Identify the blood parasite species.
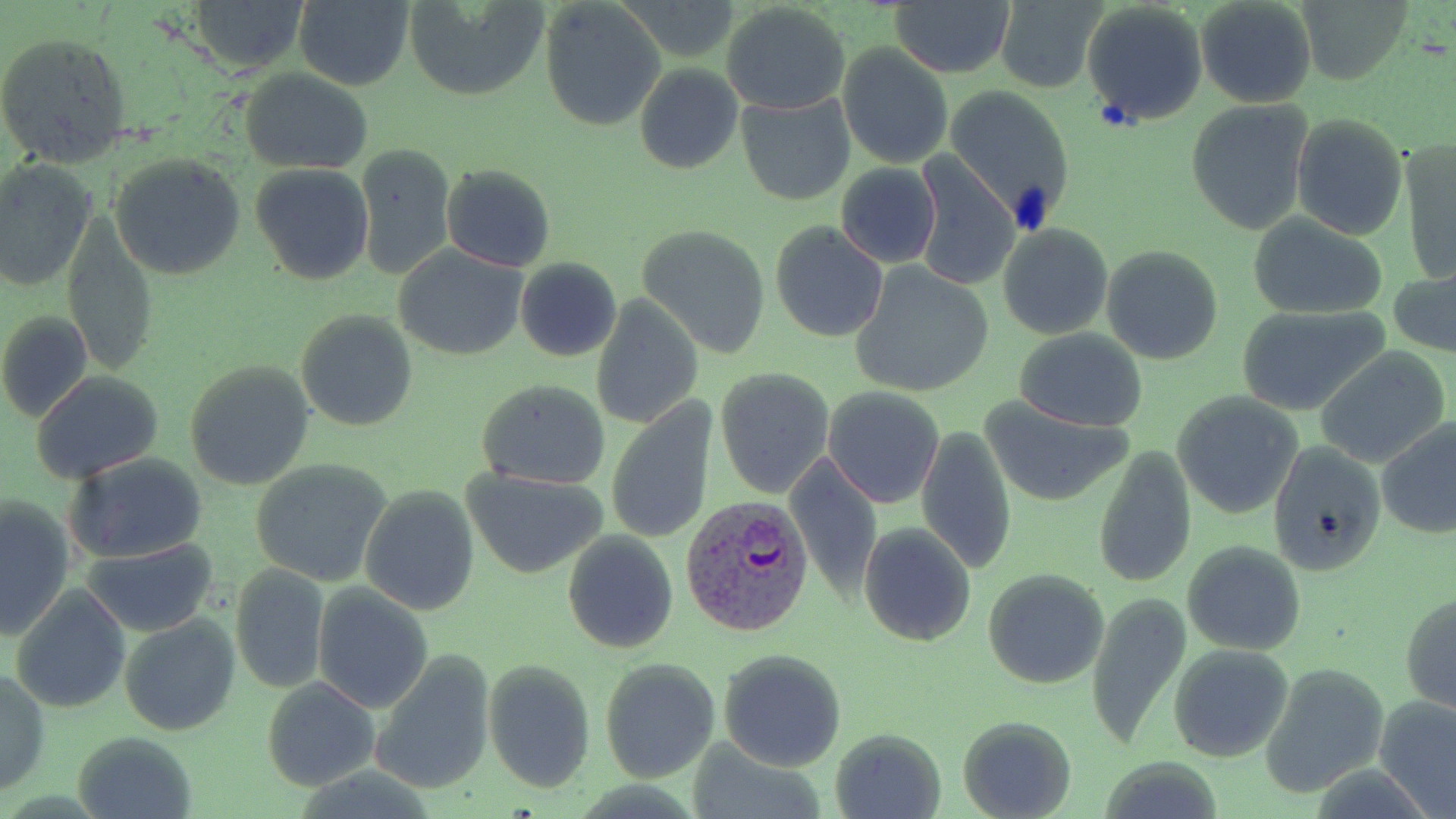

Plasmodium vivax.

Approximate bounding boxes as [x1, y1, x2, y2] in pixels. Uninfected red blood cell locations: [186, 0, 307, 74], [294, 0, 414, 91], [403, 0, 552, 101], [992, 0, 1106, 95], [1196, 0, 1319, 109], [1299, 0, 1414, 86], [889, 1, 1013, 78], [540, 2, 664, 131], [1082, 2, 1208, 128], [721, 3, 850, 114], [0, 30, 134, 170], [837, 43, 955, 170], [635, 64, 743, 175], [241, 69, 373, 174], [942, 84, 1076, 230], [735, 93, 855, 206], [1185, 99, 1314, 235], [1290, 113, 1409, 239], [1400, 138, 1455, 288], [355, 144, 458, 278], [913, 152, 1020, 294], [107, 153, 246, 281], [0, 158, 99, 293], [441, 162, 555, 273], [837, 163, 942, 268], [249, 164, 375, 285], [1248, 216, 1390, 318], [63, 217, 157, 378], [771, 221, 888, 341], [638, 222, 771, 356], [997, 223, 1113, 340], [393, 245, 528, 361], [1100, 246, 1224, 366], [514, 258, 621, 362], [848, 262, 995, 400], [1389, 270, 1456, 358], [589, 294, 704, 430], [1236, 303, 1390, 416], [0, 309, 93, 424], [296, 309, 418, 432], [1013, 329, 1148, 432], [1313, 345, 1451, 468], [182, 361, 314, 491], [714, 366, 835, 498], [31, 372, 165, 482], [476, 378, 611, 489], [822, 385, 946, 511], [1172, 392, 1305, 521], [979, 397, 1137, 507], [606, 401, 718, 545], [1376, 419, 1456, 538], [916, 427, 1016, 573], [1267, 440, 1387, 575], [1093, 446, 1198, 589], [64, 452, 209, 564], [785, 456, 883, 601], [249, 458, 392, 586], [461, 468, 608, 579], [360, 483, 482, 616], [1, 495, 75, 640], [859, 523, 975, 646], [562, 530, 679, 654], [81, 539, 220, 638], [1182, 540, 1306, 655], [231, 563, 330, 695], [981, 567, 1109, 689], [10, 584, 132, 714], [312, 584, 433, 714], [1401, 590, 1456, 715], [1086, 592, 1191, 749], [118, 614, 240, 737], [1169, 643, 1295, 763], [718, 648, 848, 770], [367, 650, 496, 795], [600, 657, 720, 783], [482, 658, 595, 792], [1262, 661, 1388, 797], [0, 667, 50, 796], [262, 676, 381, 791], [1375, 694, 1456, 818], [958, 715, 1077, 819], [830, 728, 945, 818], [72, 732, 197, 819], [684, 742, 827, 818]. Plasmodium vivax-infected red blood cell locations: [682, 495, 817, 639]. Image is 1456×819 pixels. Optical microscopy. Thin blood film. 1000x magnification. One field of a larger specimen. May-Grünwald-Giemsa stain.